Report the malaria status of this cell.
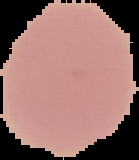
It is uninfected.

From a thin blood film. Image is 139×160 pixels. The area outside the segmented cell region is set to black.